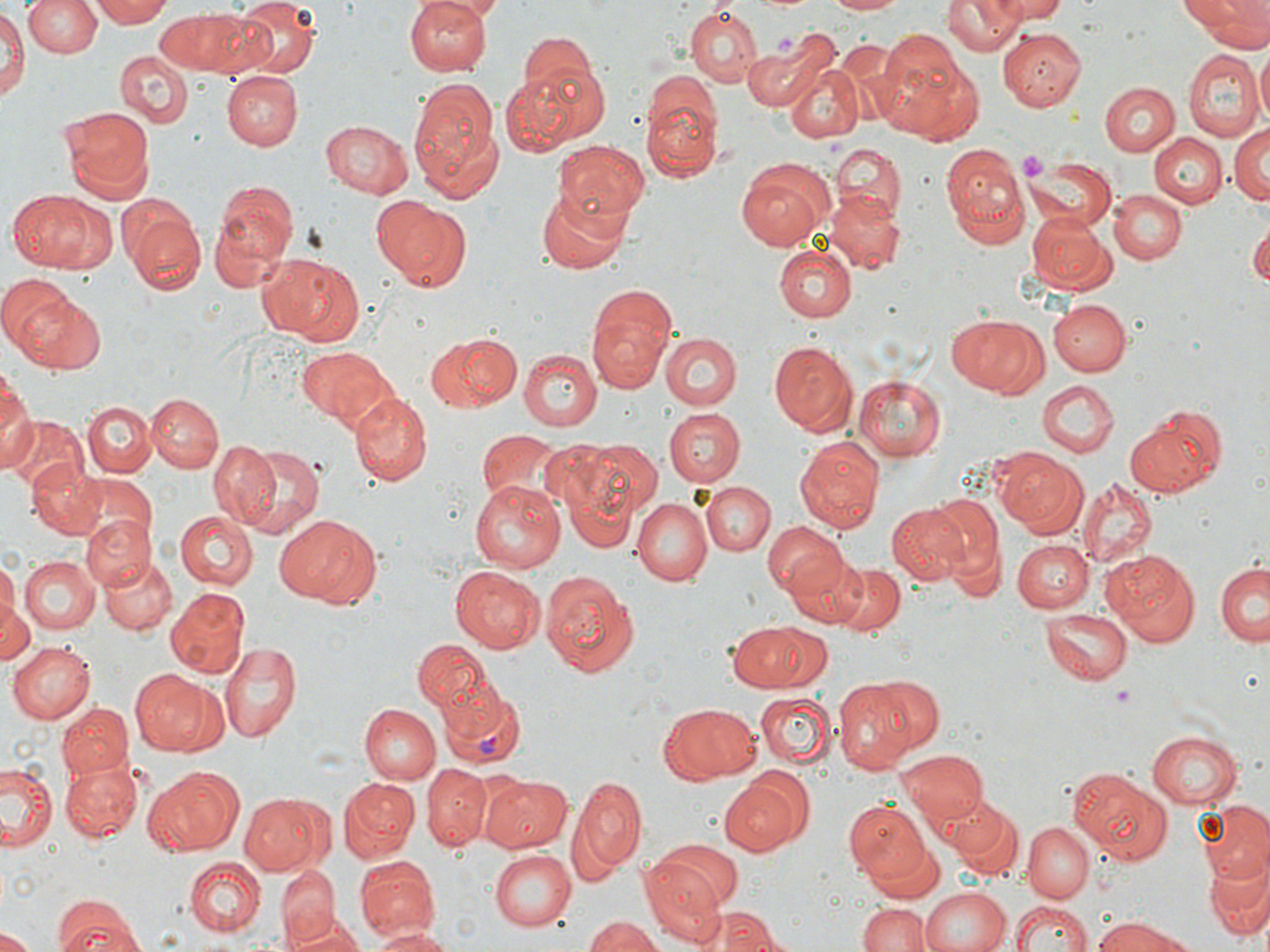 Approximate bounding boxes as (x1,y1)-(x2,y2) corner pairs in pixels. Plasmodium vivax-infected red blood cell locations: (436,680)-(526,770). Platelet locations: (775,34)-(796,60), (1019,151)-(1047,183), (1114,684)-(1137,712). Uninfected red blood cell locations: (26,0)-(100,59), (91,0)-(175,27), (233,0)-(319,81), (405,0)-(493,73), (426,0)-(509,20), (741,0)-(823,14), (828,0)-(904,15), (944,0)-(1021,54), (991,0)-(1068,23), (1183,0)-(1268,46), (0,5)-(26,107), (155,6)-(252,79), (686,8)-(760,85), (998,29)-(1085,111), (514,31)-(600,107), (875,31)-(981,142), (748,40)-(830,118), (1256,46)-(1270,131), (115,51)-(194,129), (1183,51)-(1260,138), (510,53)-(612,151), (784,60)-(866,143), (221,70)-(300,148), (408,74)-(501,201), (643,77)-(725,183), (1100,82)-(1176,155), (60,107)-(152,197), (319,119)-(414,199), (1229,124)-(1270,206), (1149,132)-(1224,207), (552,141)-(652,227), (941,142)-(1031,250), (830,145)-(908,223), (735,156)-(835,250), (1026,157)-(1117,232), (210,179)-(298,285), (537,187)-(637,274), (10,189)-(102,272), (824,190)-(905,274), (1108,190)-(1187,265), (367,195)-(470,294), (122,206)-(208,296), (1026,211)-(1114,292), (1249,225)-(1270,289), (774,244)-(858,324), (256,252)-(365,346), (0,275)-(70,354), (5,286)-(104,376), (586,299)-(676,394), (1050,300)-(1131,376), (948,313)-(1048,398), (423,331)-(521,411), (663,331)-(742,409), (770,341)-(858,436), (295,345)-(395,428), (519,349)-(601,430), (854,375)-(947,460), (0,376)-(35,472), (1039,380)-(1117,457), (349,391)-(432,485), (145,393)-(223,473), (83,399)-(155,478), (1126,407)-(1225,496), (663,408)-(746,486), (2,415)-(88,497), (475,429)-(574,510), (794,437)-(883,534), (573,439)-(663,521), (209,440)-(284,529), (233,446)-(326,536), (992,447)-(1087,533), (26,462)-(106,538), (1077,478)-(1155,569), (470,481)-(565,573), (702,482)-(774,557), (696,485)-(825,573), (922,495)-(1003,590), (633,499)-(712,586), (887,503)-(971,585), (174,511)-(258,589), (80,513)-(155,591), (274,514)-(377,607), (761,524)-(847,600), (1011,538)-(1091,612), (1104,549)-(1199,644), (786,554)-(867,629), (18,555)-(99,633), (100,556)-(176,636), (1,559)-(18,638), (829,563)-(904,636), (1215,563)-(1268,645), (451,566)-(543,653), (542,572)-(639,677), (165,588)-(250,678), (1,597)-(37,665), (1040,608)-(1130,684), (728,621)-(824,690), (413,638)-(490,709), (8,641)-(96,724), (219,642)-(302,741), (131,671)-(228,758), (873,677)-(943,749), (832,680)-(919,771), (755,694)-(839,769), (359,701)-(453,853), (664,702)-(760,783), (57,703)-(133,779), (361,705)-(440,784), (1149,731)-(1243,807), (897,750)-(987,825), (60,760)-(144,841), (2,762)-(59,852), (422,765)-(491,849), (1066,766)-(1173,865), (143,769)-(239,856), (483,775)-(573,853), (571,776)-(647,871), (719,776)-(801,854), (337,778)-(419,862), (237,792)-(330,878), (938,798)-(1024,884), (842,799)-(929,884), (1194,802)-(1269,880), (1023,822)-(1094,900), (864,831)-(947,904), (650,837)-(743,912), (489,848)-(577,932), (1203,852)-(1270,944), (187,856)-(266,936), (357,857)-(439,941), (640,857)-(724,941), (277,870)-(341,946), (920,886)-(1010,952), (53,898)-(147,951), (1010,899)-(1095,952), (859,901)-(929,952), (712,912)-(784,952), (287,916)-(365,952), (584,917)-(667,952), (1090,917)-(1192,952), (368,926)-(452,952), (0,930)-(35,952). Slide-level diagnosis: Plasmodium vivax. Optical microscopy. May-Grünwald-Giemsa-stained preparation. 1000x magnification. Thin blood film. Image is 1270×952 pixels. One field of a larger specimen.